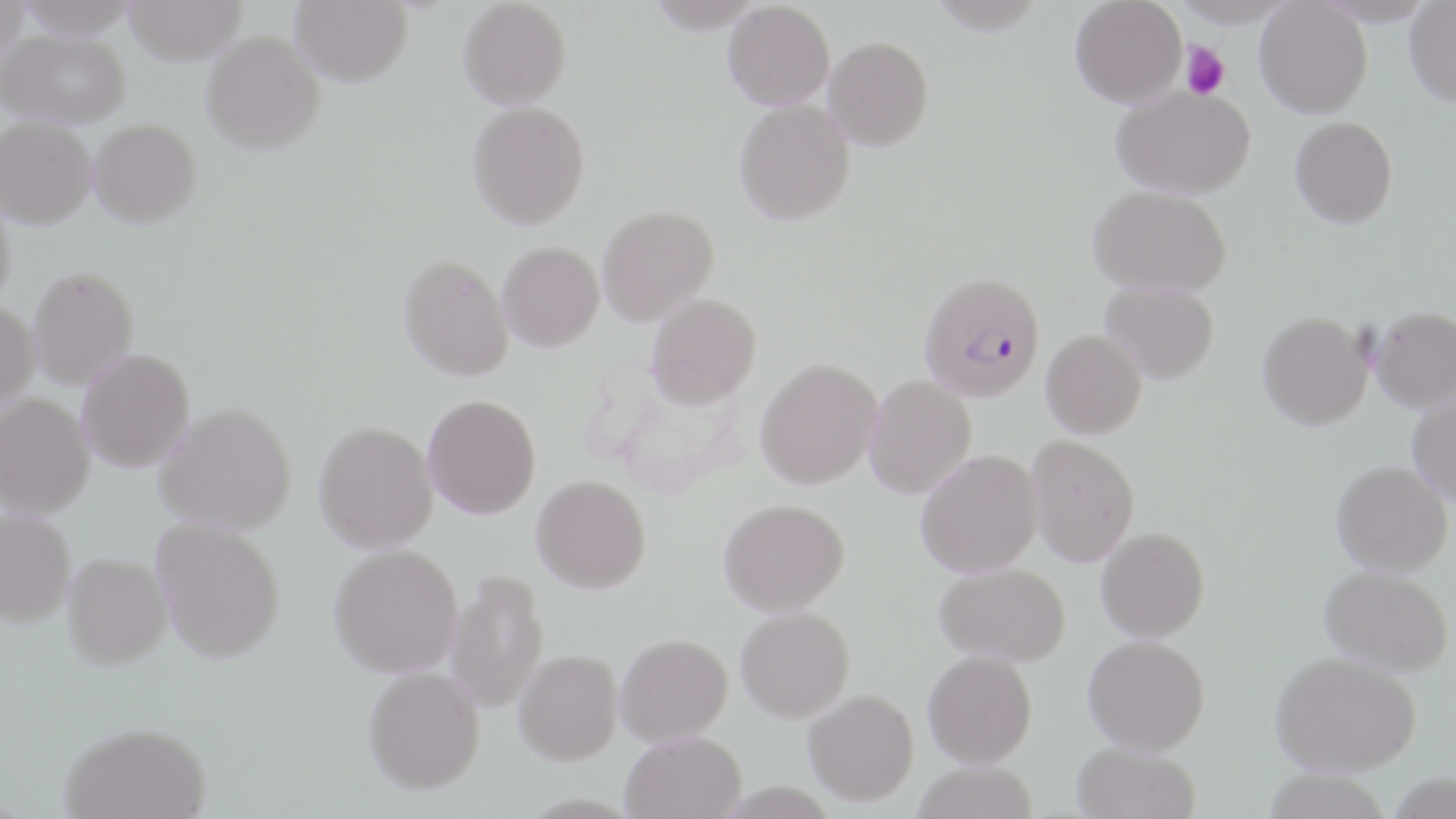
Summary:
  - Coordinate format: approximate bounding boxes as (x1,y1)-(x2,y2) corner pairs in pixels
  - Platelet locations: (1181,41)-(1230,99)
  - Plasmodium falciparum-infected red blood cell locations: (918,271)-(1045,403)
  - Uninfected red blood cell locations: (0,0)-(29,70), (15,0)-(142,39), (123,0)-(248,65), (291,0)-(412,86), (458,0)-(571,109), (646,0)-(765,33), (927,0)-(1046,35), (1070,0)-(1187,107), (1171,0)-(1297,27), (1254,0)-(1373,118), (723,1)-(835,110), (1403,2)-(1456,106), (2,28)-(130,128), (201,31)-(324,154), (824,36)-(933,150), (1111,85)-(1256,199), (733,99)-(855,225), (467,101)-(590,229), (0,116)-(97,228), (1290,116)-(1398,228), (89,118)-(202,227), (1088,185)-(1232,296), (0,190)-(16,314), (597,206)-(719,325), (497,242)-(604,352), (399,254)-(513,381), (28,266)-(138,389), (1101,280)-(1219,384), (646,293)-(762,408), (0,302)-(40,417), (1370,306)-(1456,412), (1257,312)-(1373,430), (1041,330)-(1146,439), (77,348)-(195,472), (755,358)-(882,489), (864,376)-(977,499), (1408,390)-(1456,507), (1,393)-(94,518), (423,394)-(541,519), (155,403)-(296,534), (314,421)-(438,553), (1027,435)-(1140,566), (915,449)-(1043,578), (1331,461)-(1453,575), (531,475)-(651,593), (718,498)-(849,616), (0,510)-(75,627), (151,518)-(285,663), (1096,527)-(1209,642), (329,543)-(462,678), (63,553)-(172,669), (934,563)-(1070,666), (1319,565)-(1453,676), (446,570)-(549,714), (735,607)-(854,722), (615,633)-(732,745), (1083,635)-(1210,755), (514,649)-(622,764), (922,649)-(1037,768), (1271,652)-(1421,775), (363,666)-(485,794), (804,689)-(919,805), (60,721)-(212,819), (621,730)-(746,819), (1071,742)-(1200,819), (913,761)-(1038,819), (1261,768)-(1392,819)
  - Slide-level diagnosis: Plasmodium falciparum
  - Modality: optical microscopy
  - Field of view: single
  - Preparation: thin blood smear
  - Stain: May-Grünwald-Giemsa
  - Magnification: 1000x
  - Image size: 1456×819 pixels